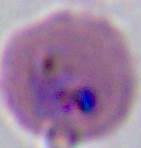
Summary:
  - Magnification: 400x or 1000x
  - Modality: photomicrograph
  - Identification: Plasmodium